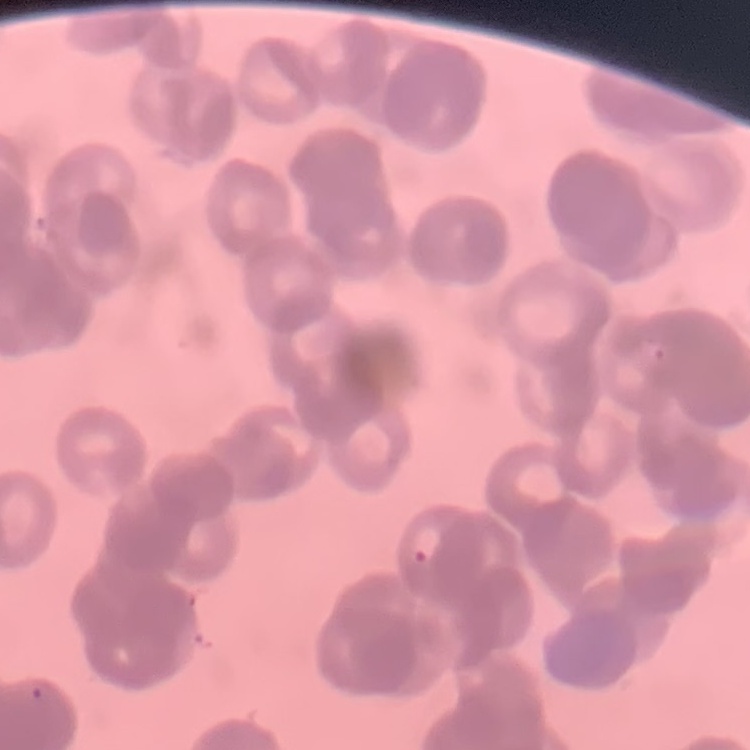

The red blood cells show rouleaux formation. Thin blood smear. Field's or Giemsa stain. One tile cut from a larger photomicrograph.